Identify the parasite.
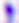
Toxoplasma gondii.

modality = photomicrograph
magnification = 400x